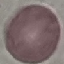

Summary:
  - Result: no malaria parasites seen
  - Preparation: thin blood film
  - Stain: Giemsa
  - Image type: automatically extracted cell patch, resized to 64 × 64 pixels
  - Capture: smartphone through the microscope eyepiece